State the preparation type.
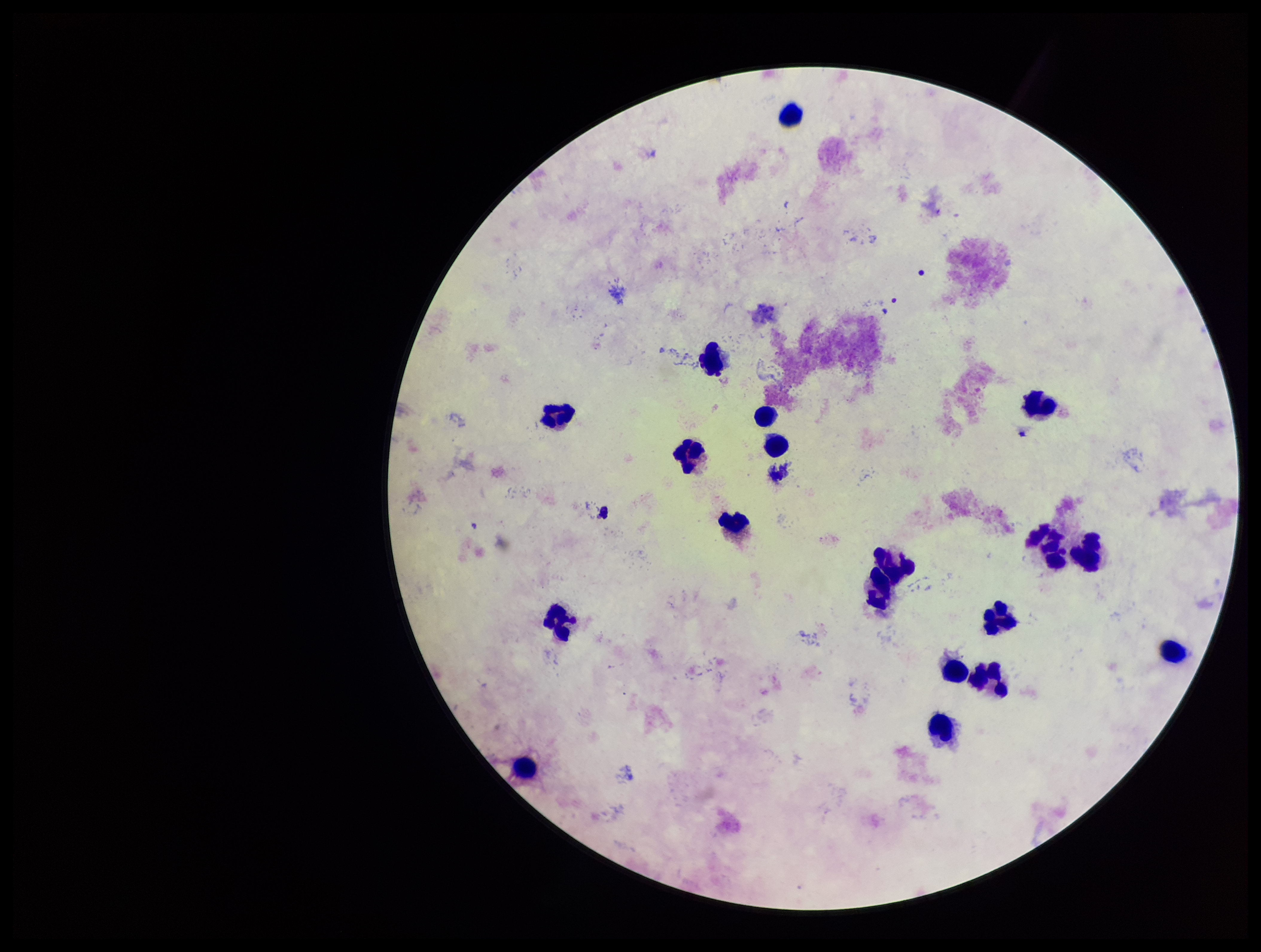
A thick smear.

Summary:
  - Capture: smartphone photograph through the microscope eyepiece
  - Leukocyte count: 19
  - Image size: 1261×952 pixels
  - Field of view: one from this slide
  - Stain: Giemsa
  - Plasmodium parasites: none detected
  - Parasite count: 0
  - Patient malaria status: negative